Classify this cell by malaria status.
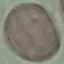
It is uninfected.

Summary:
  - Image type: automatically extracted cell patch, resized to 64 × 64 pixels
  - Capture: smartphone through the microscope eyepiece
  - Preparation: thin smear
  - Stain: Giemsa